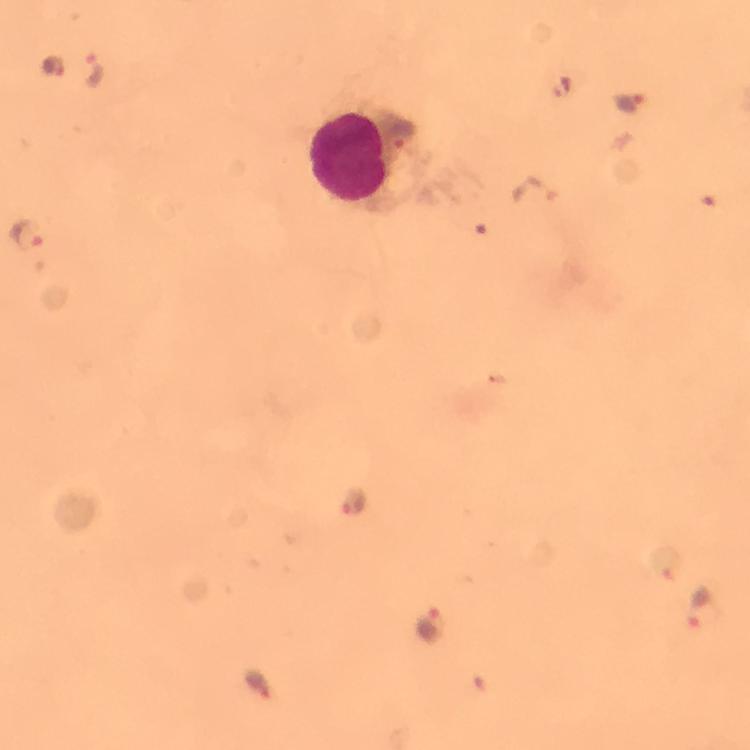
Approximate centers as (x, y) in pixels. Leukocyte locations: (349, 157). Plasmodium parasite locations: (54, 66), (92, 69), (629, 101), (402, 136), (533, 191), (25, 233), (356, 496), (698, 605), (430, 623), (257, 681). Cropped region of a single field of view. Thick blood smear. From a malaria diagnostic workup. Immersion oil applied. Photographed with a smartphone mounted on the microscope. Image is 750×750 pixels. At 100x magnification. Giemsa-stained preparation.